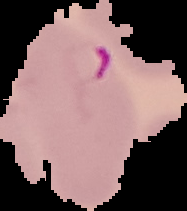
malaria status = parasitized
preparation = thin blood smear
image size = 187×211 pixels
image type = cell region segmented out of the field of view; surrounding area masked to black